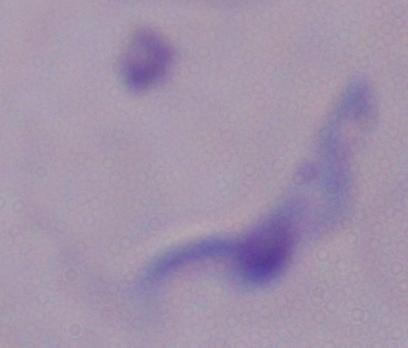
Summary:
  - Magnification: 1000x
  - Identification: trypanosome
  - Modality: photomicrograph